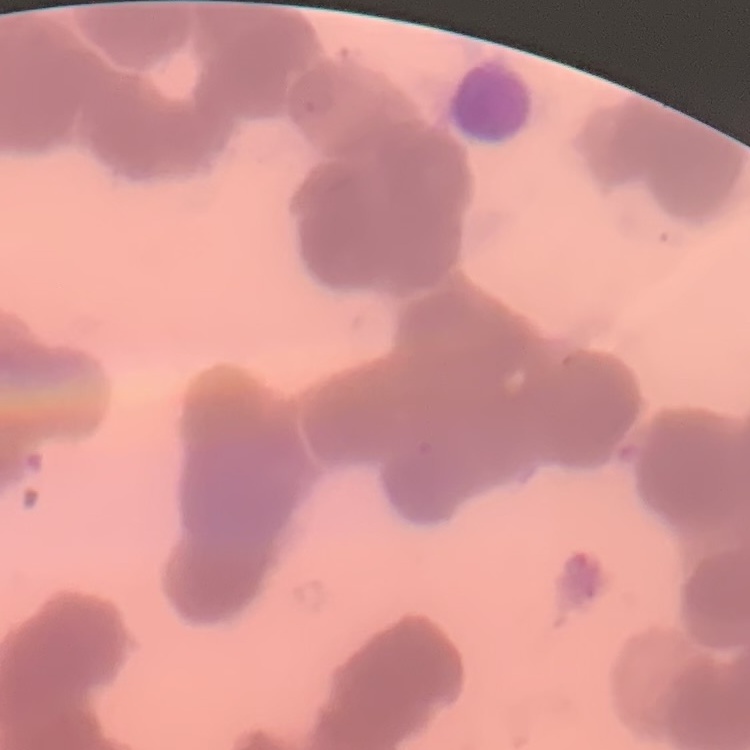
The erythrocytes show rouleaux formation. One tile cut from a larger photomicrograph. Field's or Giemsa stain. Thin peripheral smear.